Classify this cell by malaria status.
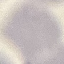

It is uninfected.

Summary:
  - Image type: cell patch, automatically extracted from a larger field of view and resized to 64 × 64 pixels
  - Stain: Giemsa
  - Preparation: thin smear
  - Capture: smartphone camera at the microscope eyepiece